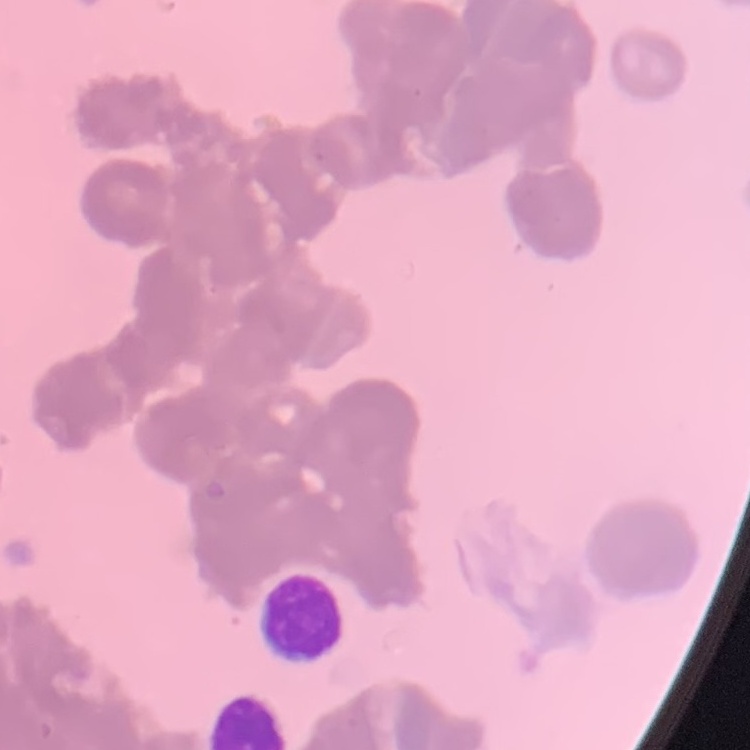 The red blood cells exhibit rouleaux formation. Thin blood film. One tile cut from a larger photomicrograph. Stained with either Field's or Giemsa.